Assess this cell for malaria.
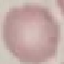
Uninfected.

Thin smear of blood. Cell patch, automatically extracted from a larger field of view and resized to 64 × 64 pixels. Acquired by smartphone through the microscope eyepiece. Giemsa-stained preparation.